Name the cell type shown.
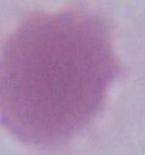

This is an erythrocyte.

modality: photomicrograph
magnification: 1000x